State the preparation type.
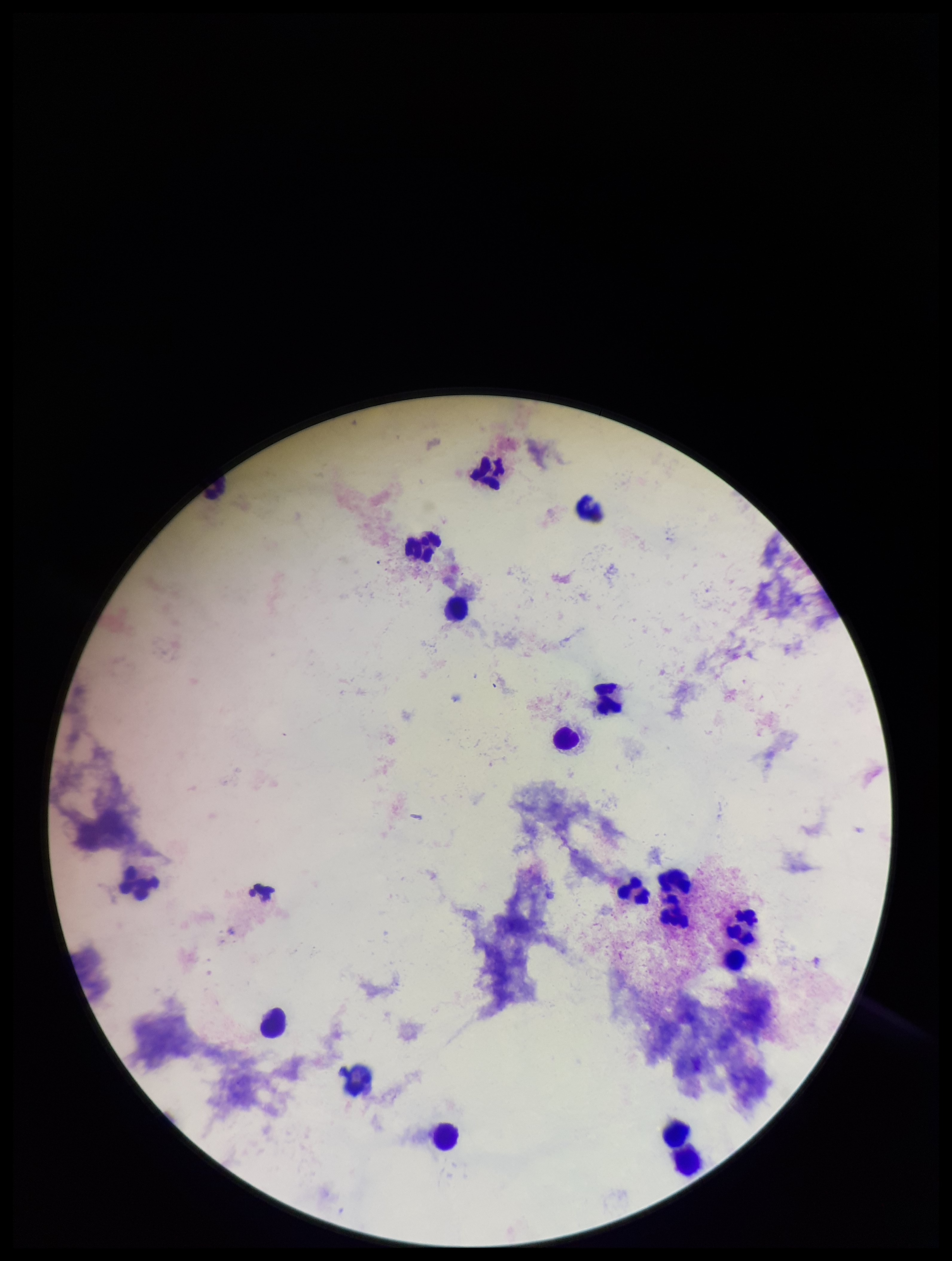

It is a thick blood smear.

parasite_count: 0
field_of_view: one from this slide
leukocyte_count: 17
stain: Giemsa
plasmodium_parasites: none identified
image_size: 952×1261 pixels
capture: smartphone photograph through the microscope eyepiece
patient_malaria_status: negative